State which cell type is depicted.
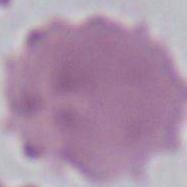

This is an erythrocyte.

magnification = 1000x
modality = micrograph